Assess the morphology of the red blood cells.
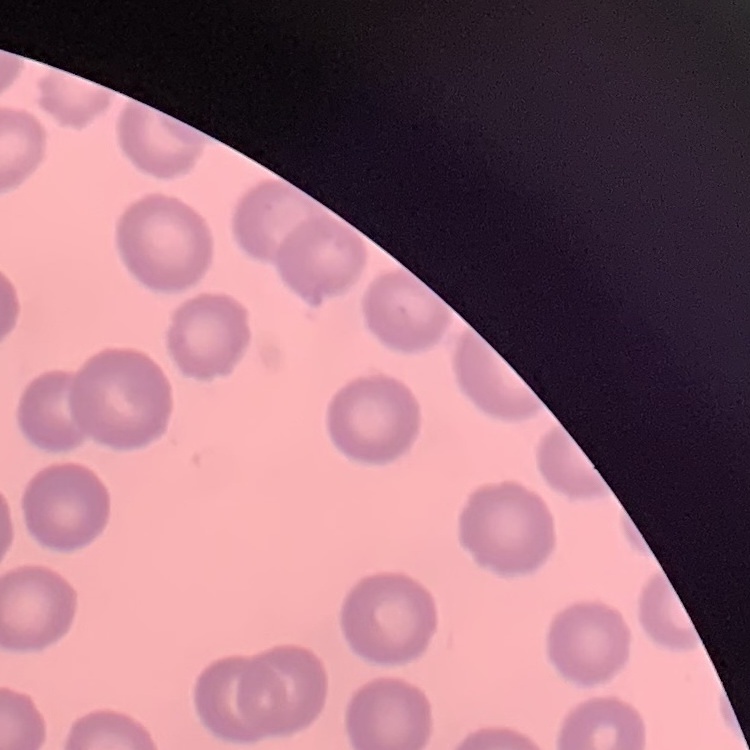
No rouleaux formation.

One tile cut from a larger photomicrograph. Stained with either Field's or Giemsa. Thin peripheral smear.